Identify the parasite.
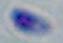
This is Toxoplasma gondii.

{
  "modality": "micrograph",
  "magnification": "1000x"
}